Outline platelets.
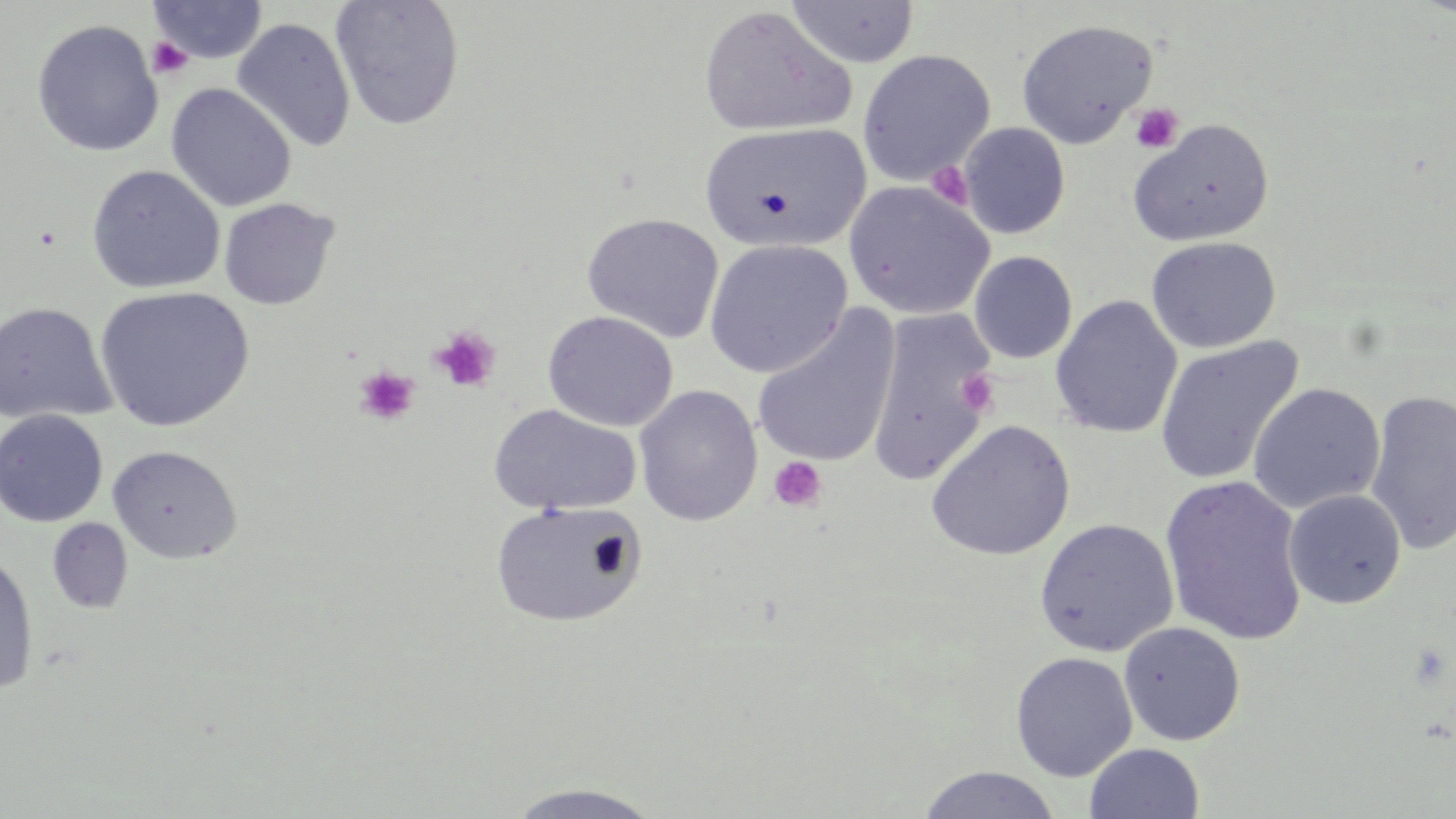
Approximate bounding boxes as (x1, y1, x2, y2) in pixels.
Platelets: (147, 37, 193, 80), (1130, 102, 1184, 154), (926, 162, 973, 209), (429, 326, 501, 393), (354, 365, 420, 426), (958, 370, 1001, 416), (768, 456, 827, 513).

Summary:
  - Uninfected red blood cell locations: (329, 0, 465, 130), (147, 1, 268, 64), (786, 1, 920, 69), (698, 5, 855, 138), (232, 18, 356, 154), (1015, 18, 1158, 149), (31, 19, 163, 157), (856, 49, 995, 185), (166, 83, 296, 212), (1127, 118, 1275, 247), (699, 122, 872, 254), (957, 122, 1070, 239), (87, 164, 225, 294), (842, 180, 995, 320), (218, 198, 340, 311), (582, 213, 724, 343), (1145, 236, 1281, 353), (703, 239, 853, 379), (969, 251, 1077, 363), (94, 285, 256, 432), (1050, 295, 1183, 438), (0, 302, 116, 425), (751, 306, 902, 469), (865, 308, 998, 486), (542, 310, 678, 431), (1155, 336, 1304, 486), (1247, 382, 1386, 514), (633, 385, 763, 526), (1365, 389, 1456, 555), (488, 404, 641, 515), (0, 409, 108, 527), (925, 418, 1076, 561), (108, 445, 243, 564), (1160, 474, 1309, 646), (1283, 489, 1406, 609), (490, 499, 647, 628), (47, 518, 133, 614), (1035, 518, 1179, 656), (0, 550, 39, 695), (1118, 621, 1246, 746), (1010, 651, 1138, 782), (1084, 743, 1205, 819), (917, 766, 1062, 819), (501, 783, 668, 818)
  - Slide-level diagnosis: negative for blood parasites
  - Preparation: thin blood film
  - Field of view: one of a larger specimen
  - Stain: May-Grünwald-Giemsa
  - Magnification: 1000x
  - Modality: light microscopy
  - Image size: 1456×819 pixels